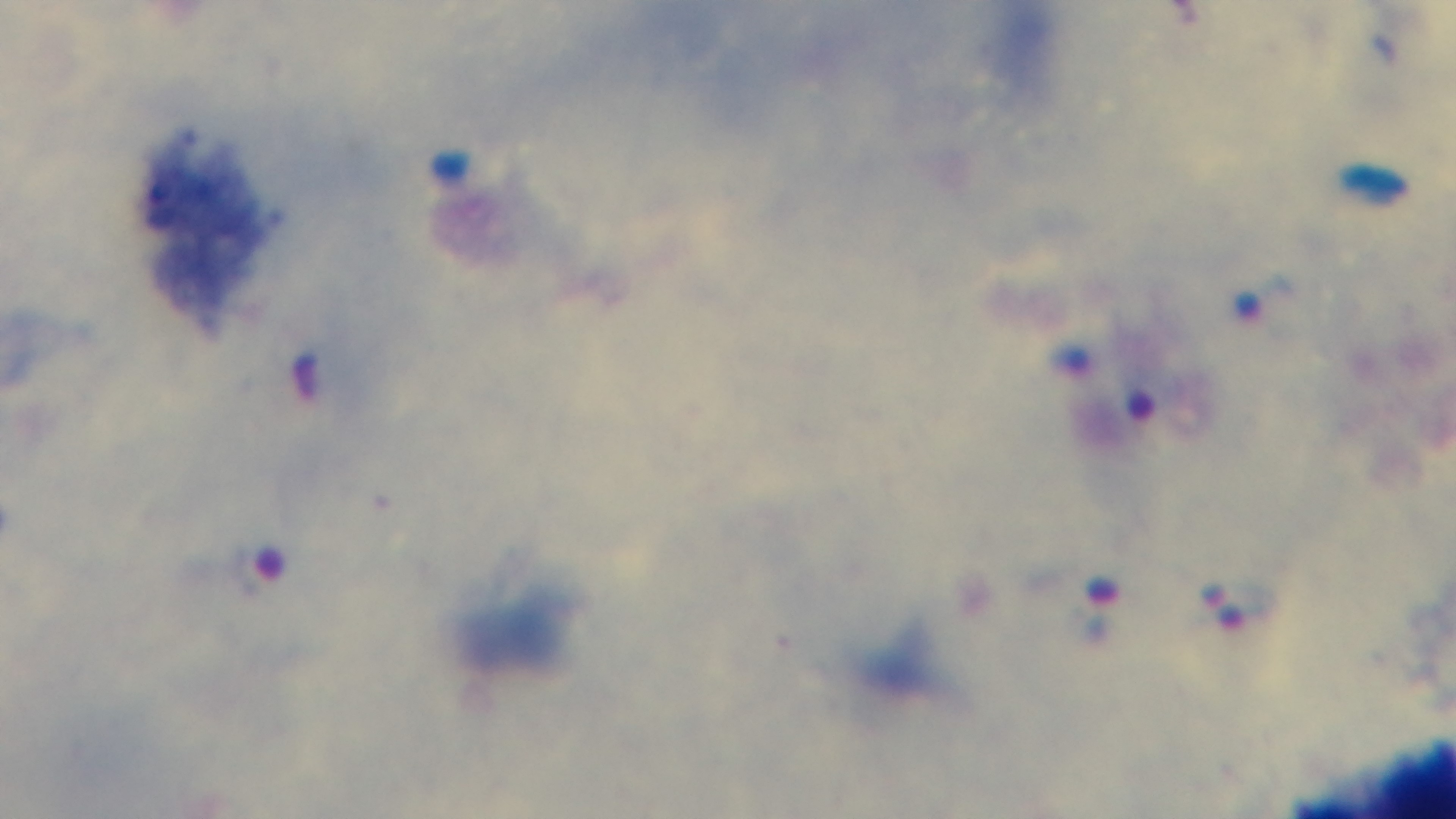
field_of_view: one from the slide
modality: light microscopy
malaria_status: positive
stain: Giemsa
objective: 100x oil immersion
capture: mounted 4K digital camera
preparation: thick smear